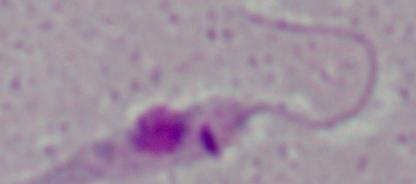
Summary:
  - Modality: micrograph
  - Magnification: 1000x
  - Identification: Leishmania